Name the parasite shown.
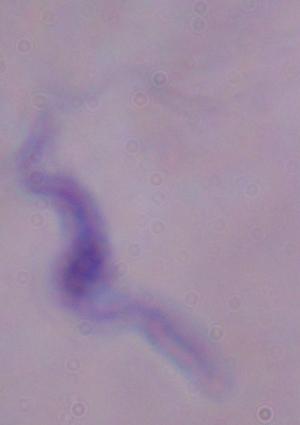
This is a trypanosome.

magnification = 1000x
modality = photomicrograph